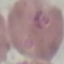
Malaria status: parasitized. Acquired by smartphone through the microscope eyepiece. Thin blood film. Giemsa stain. Automatically extracted cell patch, resized to 64 × 64 pixels.